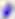

modality = photomicrograph
magnification = 400x
identification = Toxoplasma gondii